Name the parasite shown.
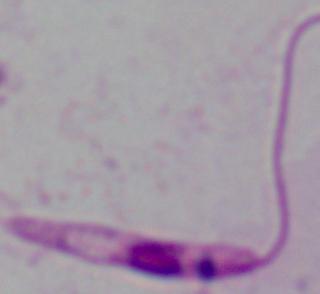
Leishmania.

Summary:
  - Modality: photomicrograph
  - Magnification: 1000x